Report the malaria status of this cell.
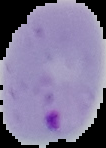

Parasitized.

Summary:
  - Preparation: thin blood film
  - Image size: 106×148 pixels
  - Image type: segmented cell region on a black background